Classify this cell by malaria status.
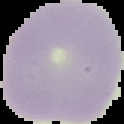

It is uninfected.

Summary:
  - Preparation: thin blood smear
  - Image size: 124×124 pixels
  - Image type: cell region segmented out of the field of view; surrounding area masked to black